Classify this cell by malaria status.
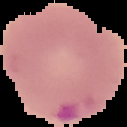

Parasitized.

From a thin blood smear. Image is 127×127 pixels. The area outside the segmented cell region is set to black.